Classify this cell by malaria status.
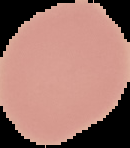
Uninfected.

Summary:
  - Image size: 130×148 pixels
  - Image type: segmented cell region on a black background
  - Preparation: thin blood film